Locate every malaria parasite.
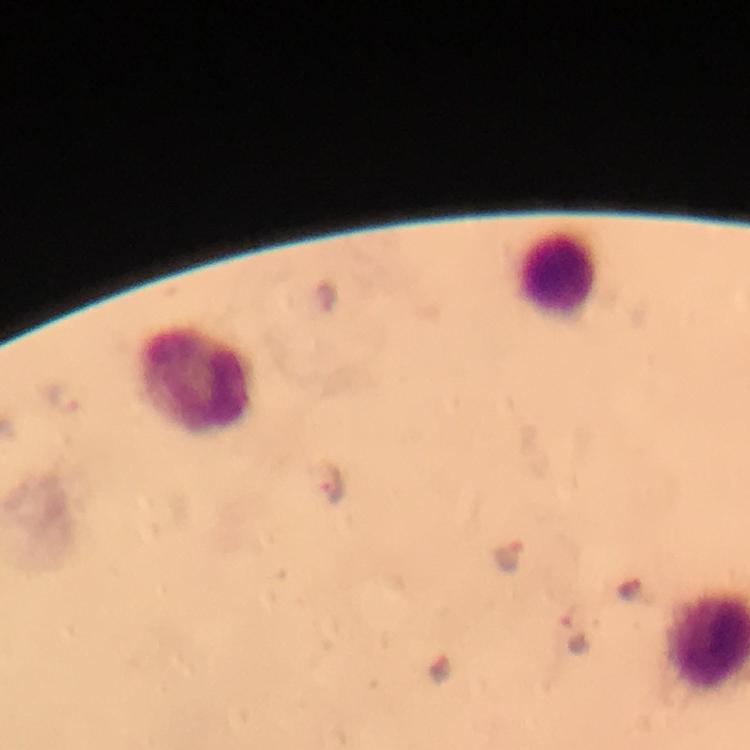

Approximate centers as {x, y} in pixels.
Malaria parasites: {67, 397}, {331, 487}, {509, 557}, {628, 587}, {575, 632}.

Summary:
  - Leukocyte locations: {557, 275}, {193, 382}
  - Capture: smartphone mounted on the microscope
  - Immersion oil: applied
  - Image size: 750×750 pixels
  - Preparation: thick blood film
  - Cropped from: one field of view
  - Magnification: 100x
  - Stain: Giemsa
  - Context: from a malaria diagnostic workup